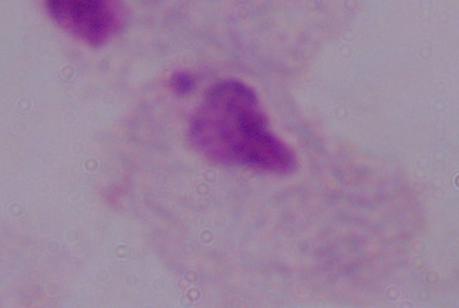
Captured at 1000x magnification. Micrograph. A trichomonad is seen.